Point out every malaria parasite and every leukocyte.
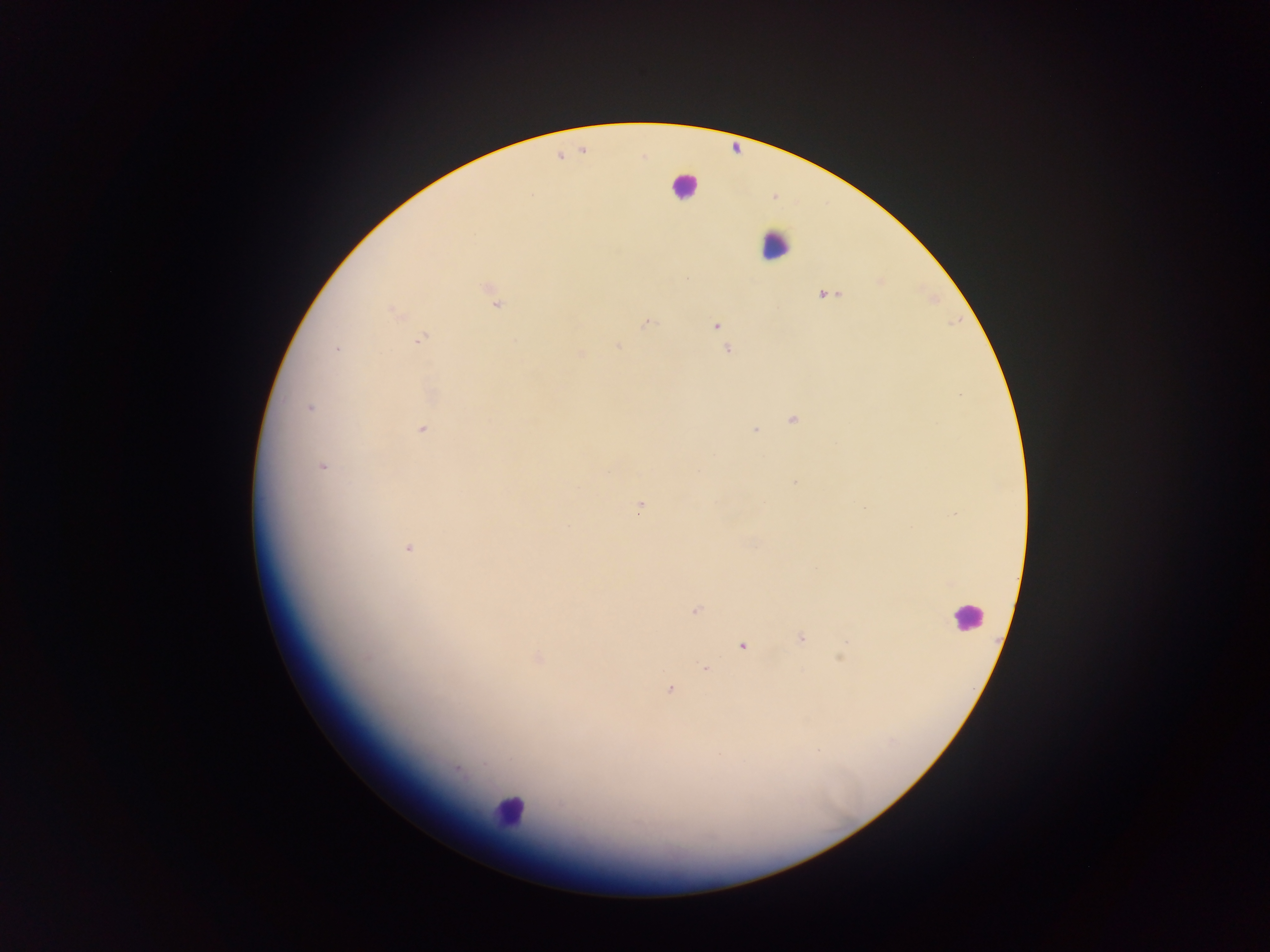

Approximate centers as {x, y} in pixels.
Malaria parasites: {490, 289}, {826, 294}, {497, 304}, {394, 313}, {647, 323}, {715, 325}, {420, 339}, {618, 346}, {336, 349}, {728, 350}, {580, 354}, {310, 407}, {792, 419}, {423, 429}, {755, 430}, {321, 466}, {794, 483}, {639, 507}, {408, 548}, {816, 569}, {694, 611}, {801, 638}, {743, 646}, {366, 657}, {840, 657}, {538, 658}, {705, 668}, {669, 690}, {485, 764}, {457, 770}.
Leukocytes: {684, 185}, {774, 244}, {967, 616}, {510, 810}.

Collected in Ghana. One field of view. Photographed through a microscope with a mobile-phone camera. Image is 1270×952 pixels. Thick blood film.